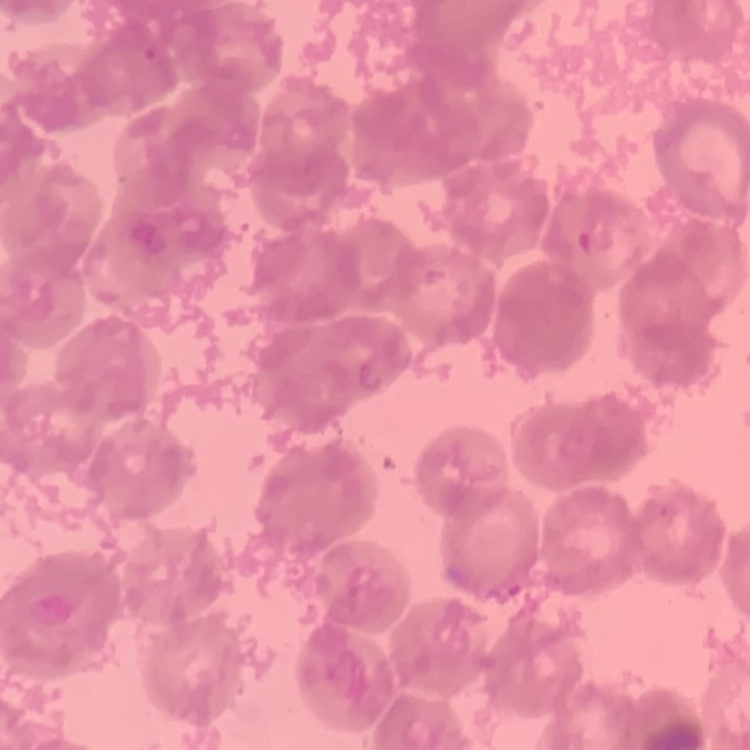
{
  "red_blood_cell_morphology": "rouleaux formation",
  "stain": "Field's or Giemsa",
  "preparation": "thin blood smear",
  "image_type": "one tile cut from a larger photomicrograph"
}